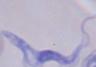
Micrograph. 1000x magnification. A trypanosome is shown.